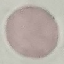
{
  "result": "negative for malaria parasites",
  "image_type": "cell patch, automatically extracted from a larger field of view and resized to 64 × 64 pixels",
  "stain": "Giemsa",
  "capture": "smartphone camera at the microscope eyepiece",
  "preparation": "thin smear"
}